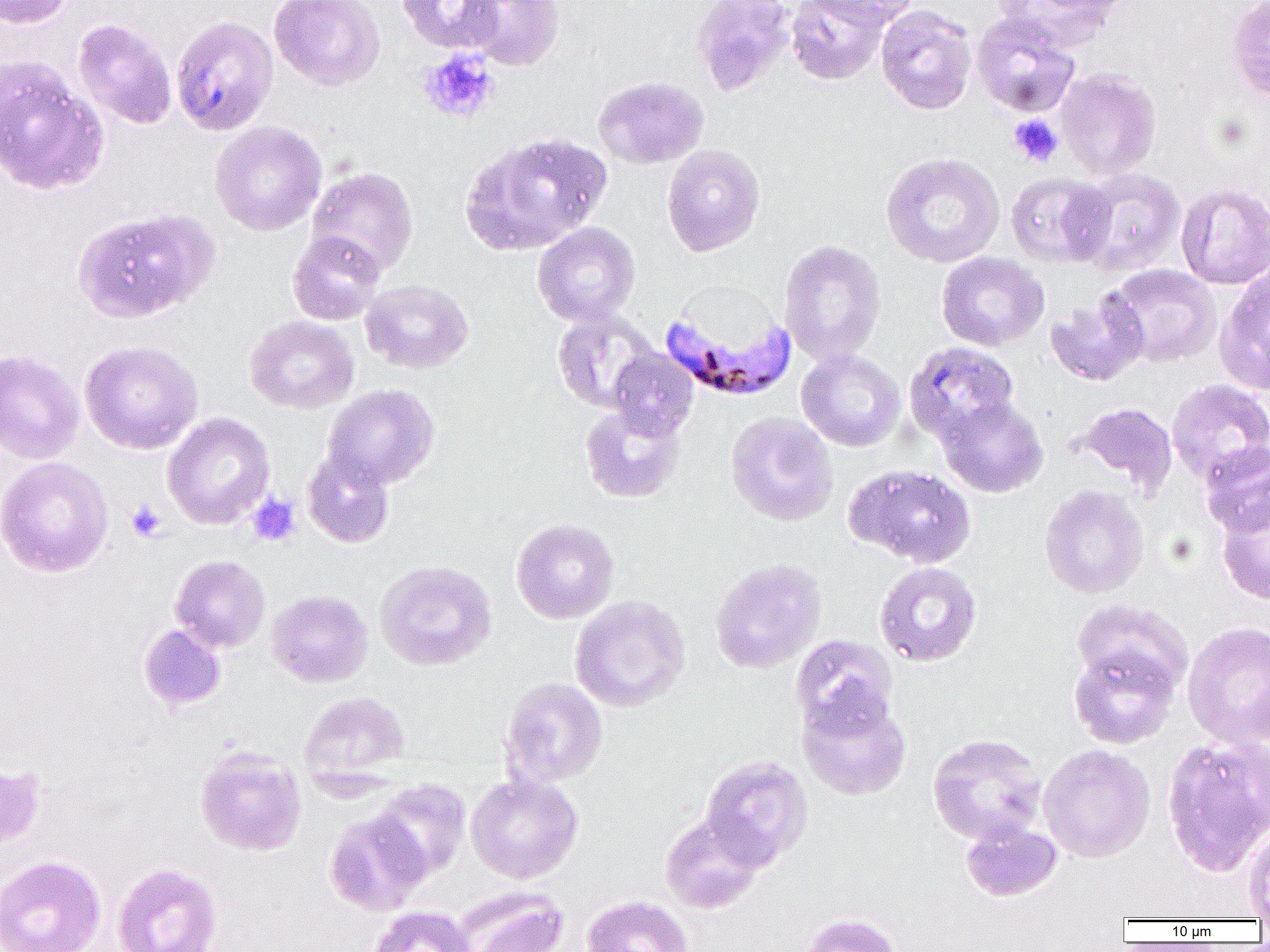
slide-level diagnosis = Plasmodium falciparum
magnification = 1000x
modality = optical microscopy
uninfected red blood cell locations = approximate bounding boxes as named x1/y1/x2/y2 corners in pixels: (x1=0, y1=0, x2=76, y2=29), (x1=269, y1=0, x2=385, y2=91), (x1=396, y1=0, x2=502, y2=54), (x1=462, y1=0, x2=565, y2=71), (x1=691, y1=0, x2=795, y2=96), (x1=786, y1=0, x2=889, y2=85), (x1=811, y1=0, x2=917, y2=29), (x1=990, y1=0, x2=1128, y2=51), (x1=1225, y1=0, x2=1270, y2=104), (x1=876, y1=4, x2=977, y2=116), (x1=971, y1=12, x2=1080, y2=117), (x1=170, y1=16, x2=278, y2=135), (x1=73, y1=19, x2=177, y2=130), (x1=0, y1=56, x2=108, y2=196), (x1=1055, y1=67, x2=1161, y2=180), (x1=592, y1=75, x2=709, y2=170), (x1=210, y1=121, x2=327, y2=236), (x1=460, y1=130, x2=612, y2=256), (x1=662, y1=144, x2=765, y2=256), (x1=880, y1=152, x2=1005, y2=268), (x1=305, y1=166, x2=418, y2=276), (x1=1074, y1=167, x2=1186, y2=276), (x1=1004, y1=172, x2=1114, y2=268), (x1=1175, y1=181, x2=1270, y2=289), (x1=72, y1=207, x2=217, y2=324), (x1=532, y1=222, x2=640, y2=327), (x1=287, y1=231, x2=386, y2=326), (x1=778, y1=239, x2=886, y2=366), (x1=936, y1=252, x2=1049, y2=351), (x1=1214, y1=262, x2=1270, y2=396), (x1=1105, y1=264, x2=1222, y2=368), (x1=360, y1=279, x2=474, y2=373), (x1=1045, y1=291, x2=1149, y2=387), (x1=551, y1=310, x2=660, y2=414), (x1=244, y1=315, x2=359, y2=414), (x1=79, y1=340, x2=204, y2=454), (x1=904, y1=341, x2=1020, y2=445), (x1=0, y1=348, x2=84, y2=464), (x1=607, y1=349, x2=698, y2=440), (x1=796, y1=349, x2=906, y2=452), (x1=1167, y1=379, x2=1270, y2=485), (x1=321, y1=384, x2=440, y2=491), (x1=937, y1=395, x2=1049, y2=498), (x1=579, y1=402, x2=685, y2=503), (x1=1075, y1=402, x2=1178, y2=496), (x1=725, y1=411, x2=838, y2=527), (x1=162, y1=412, x2=275, y2=529), (x1=1199, y1=442, x2=1270, y2=538), (x1=302, y1=450, x2=395, y2=548), (x1=0, y1=456, x2=114, y2=578), (x1=845, y1=464, x2=977, y2=568), (x1=1039, y1=484, x2=1149, y2=598), (x1=1216, y1=499, x2=1270, y2=606), (x1=511, y1=519, x2=619, y2=624), (x1=170, y1=555, x2=270, y2=653), (x1=709, y1=558, x2=826, y2=674), (x1=375, y1=560, x2=497, y2=670), (x1=874, y1=562, x2=982, y2=667), (x1=267, y1=589, x2=373, y2=688), (x1=569, y1=595, x2=690, y2=712), (x1=1070, y1=599, x2=1193, y2=699), (x1=1182, y1=621, x2=1270, y2=750), (x1=138, y1=623, x2=227, y2=713), (x1=791, y1=634, x2=899, y2=738), (x1=1068, y1=642, x2=1181, y2=749), (x1=500, y1=677, x2=608, y2=788), (x1=299, y1=691, x2=410, y2=785), (x1=797, y1=692, x2=912, y2=800), (x1=927, y1=733, x2=1047, y2=845), (x1=1161, y1=734, x2=1270, y2=877), (x1=1038, y1=744, x2=1155, y2=863), (x1=194, y1=747, x2=307, y2=856), (x1=699, y1=755, x2=813, y2=869), (x1=0, y1=760, x2=46, y2=853), (x1=466, y1=772, x2=583, y2=883), (x1=372, y1=779, x2=472, y2=881), (x1=324, y1=809, x2=431, y2=915), (x1=660, y1=814, x2=767, y2=913), (x1=961, y1=819, x2=1063, y2=902), (x1=1242, y1=825, x2=1270, y2=919), (x1=0, y1=855, x2=106, y2=952), (x1=112, y1=861, x2=222, y2=952), (x1=453, y1=885, x2=568, y2=952), (x1=582, y1=895, x2=694, y2=952), (x1=368, y1=905, x2=477, y2=952), (x1=796, y1=912, x2=904, y2=952)
platelet locations = approximate bounding boxes as named x1/y1/x2/y2 corners in pixels: (x1=417, y1=48, x2=500, y2=124), (x1=1008, y1=114, x2=1063, y2=166), (x1=246, y1=493, x2=300, y2=547), (x1=125, y1=500, x2=167, y2=543)
preparation = thin blood film
Plasmodium falciparum-infected red blood cell locations = approximate bounding boxes as named x1/y1/x2/y2 corners in pixels: (x1=659, y1=299, x2=796, y2=402)
image size = 1270×952 pixels
field of view = one of a larger specimen